Classify this cell by malaria status.
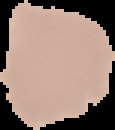
It is uninfected.

Summary:
  - Image type: segmented cell region on a black background
  - Image size: 115×130 pixels
  - Preparation: thin blood film